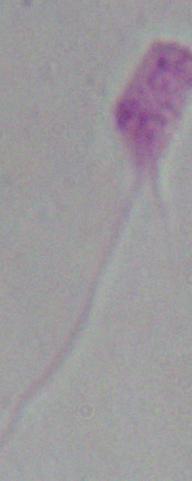
Summary:
  - Magnification: 1000x
  - Modality: micrograph
  - Identification: Leishmania